Give the position of every leukocyte visible.
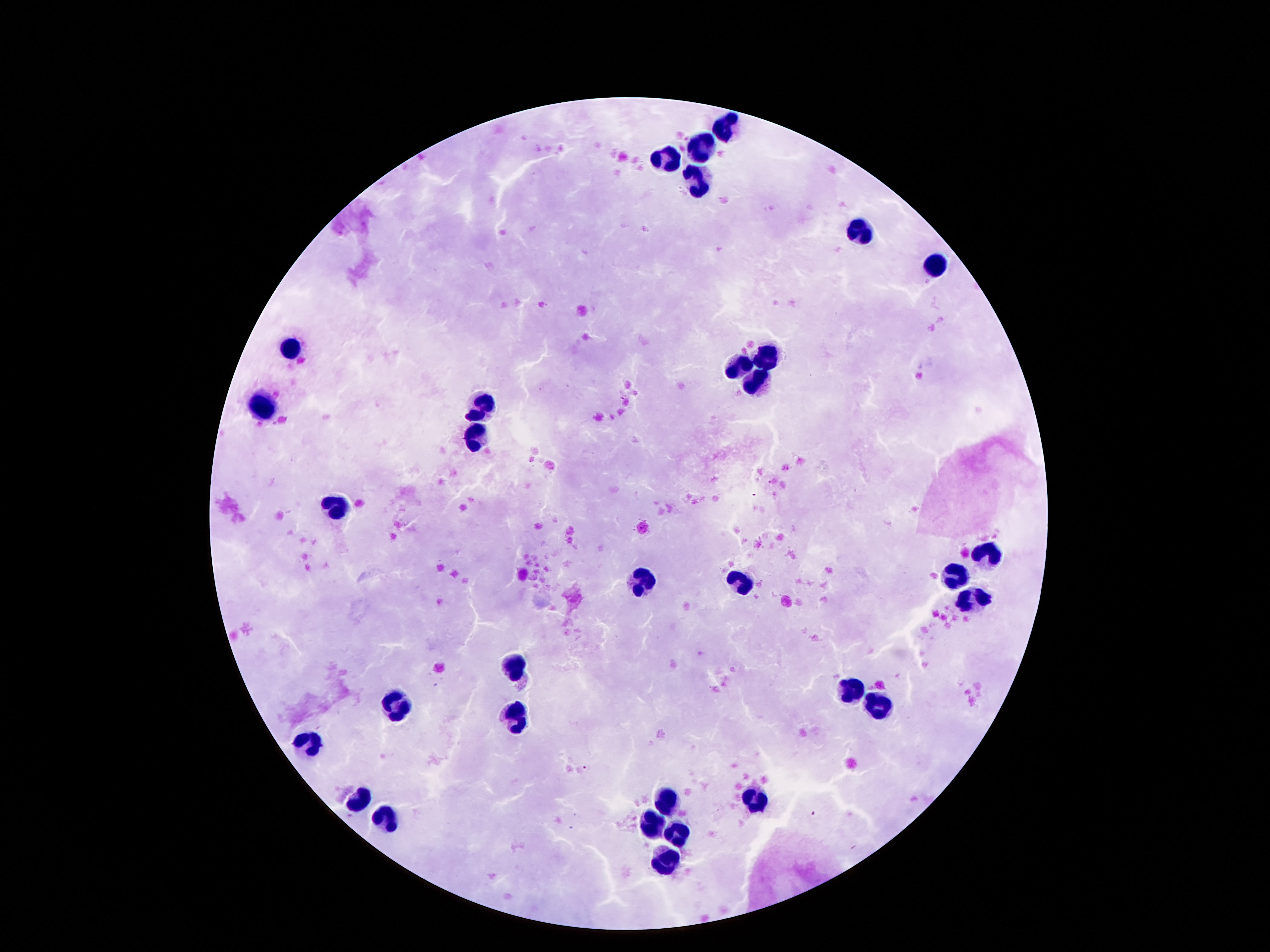
Approximate centers as (x, y) in pixels.
Leukocytes: (726, 125), (701, 145), (665, 158), (695, 179), (859, 229), (934, 267), (291, 349), (770, 353), (743, 367), (758, 386), (266, 404), (482, 406), (474, 435), (338, 506), (987, 553), (955, 578), (646, 584), (743, 584), (972, 599), (516, 668), (859, 689), (880, 706), (396, 708), (516, 717), (306, 745), (756, 796), (667, 797), (359, 798), (384, 819), (655, 823), (676, 836), (665, 855).

{
  "magnification": "100x",
  "preparation": "thick blood film",
  "stain": "Giemsa",
  "patient_malaria_status": "uninfected",
  "image_size": "1270×952 pixels",
  "field_of_view": "single",
  "capture": "smartphone camera through the microscope eyepiece"
}